Assess this cell for malaria.
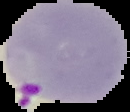

It is parasitized.

The area outside the segmented cell region is set to black. Image is 130×112 pixels. From a thin blood film.